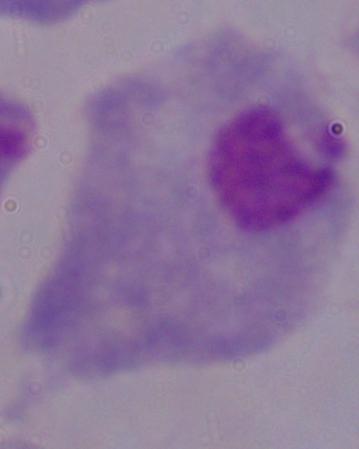
{
  "identification": "trichomonad",
  "modality": "photomicrograph",
  "magnification": "1000x"
}